Report the malaria status of this cell.
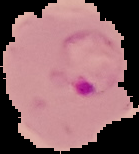
It is parasitized.

Summary:
  - Image size: 139×154 pixels
  - Image type: segmented cell region with the area outside set to black
  - Preparation: thin blood film